Comment on the morphology of the erythrocytes.
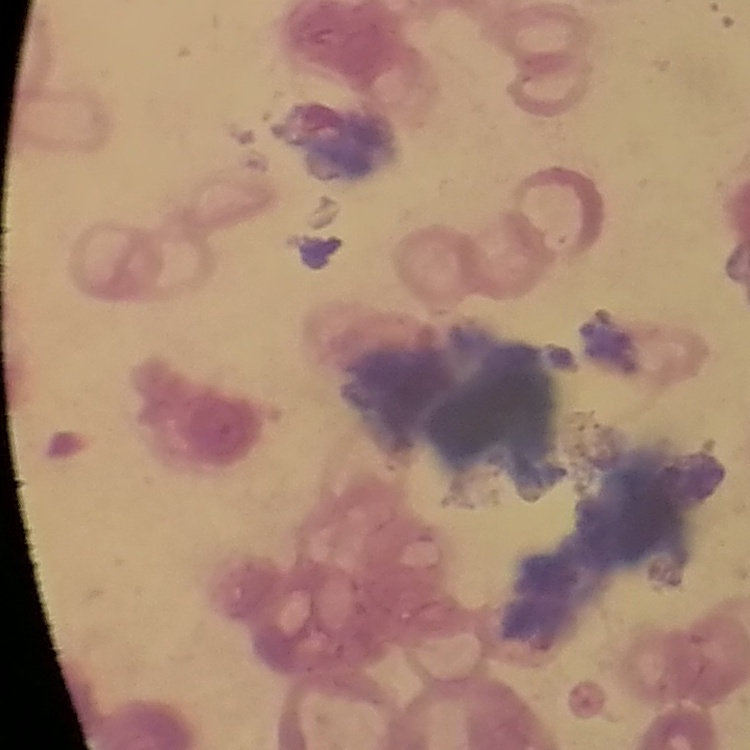
They show rouleaux formation.

{
  "image_type": "square crop of a larger photomicrograph",
  "preparation": "thin peripheral smear",
  "stain": "Field's or Giemsa"
}